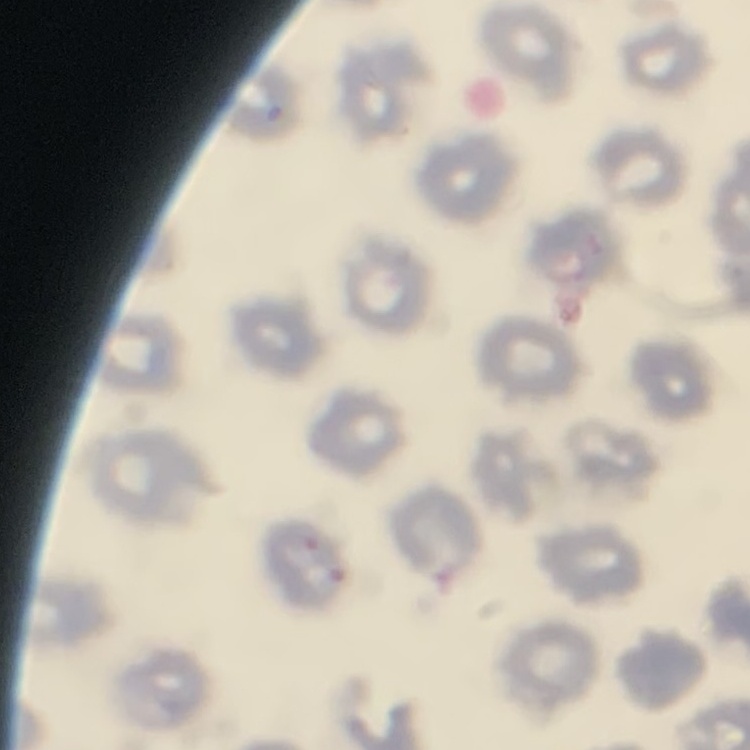

The erythrocytes show no rouleaux formation. Stained with either Field's or Giemsa. Square crop of a larger photomicrograph. Thin blood smear.